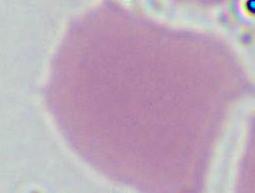
{
  "identification": "red blood cell",
  "modality": "micrograph",
  "magnification": "1000x"
}